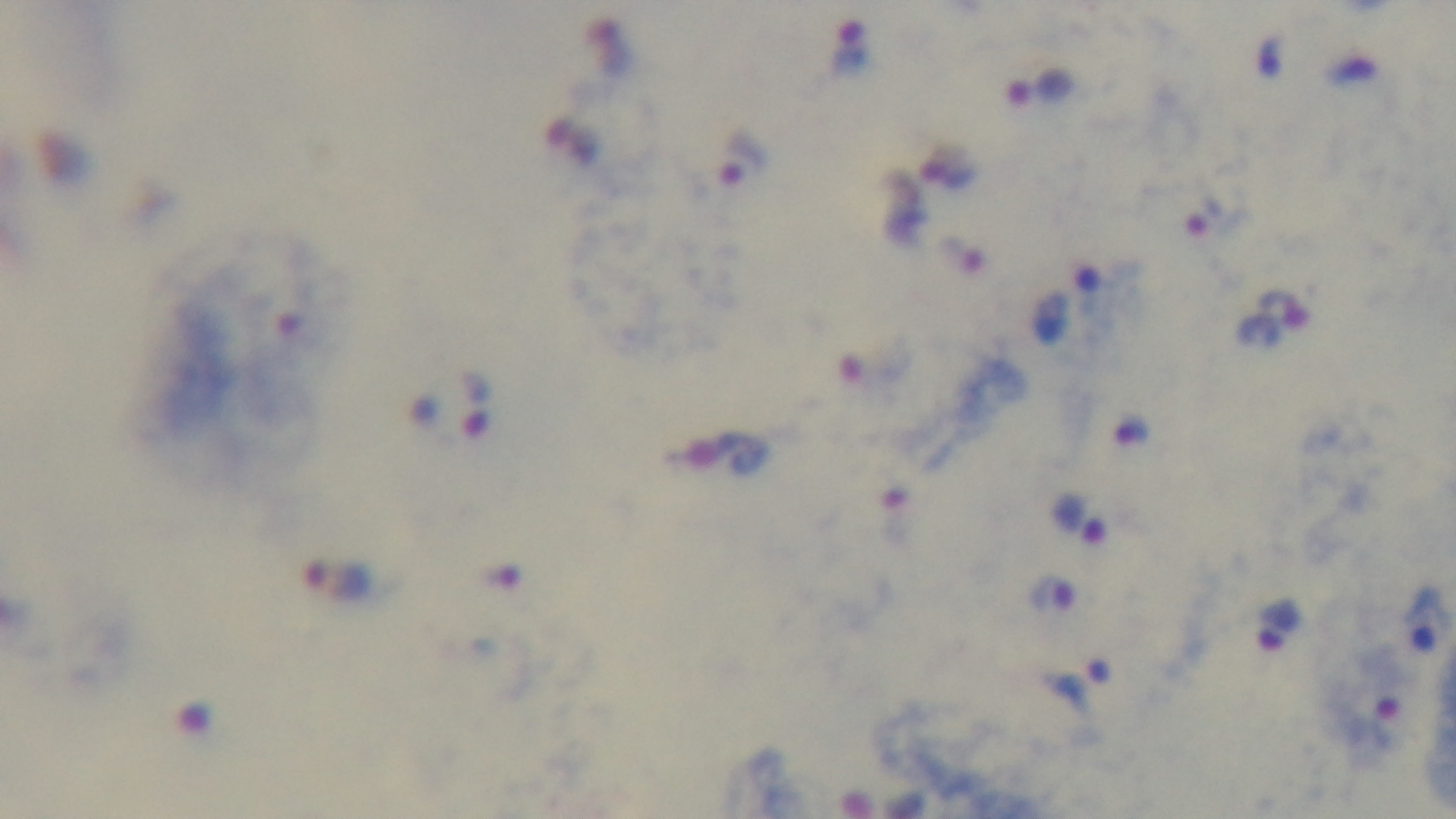 Single field of view. 100x oil-immersion objective. Malaria status: infected. Light microscopy. Mounted 4K digital camera. Giemsa stain. Preparation: thick blood film.